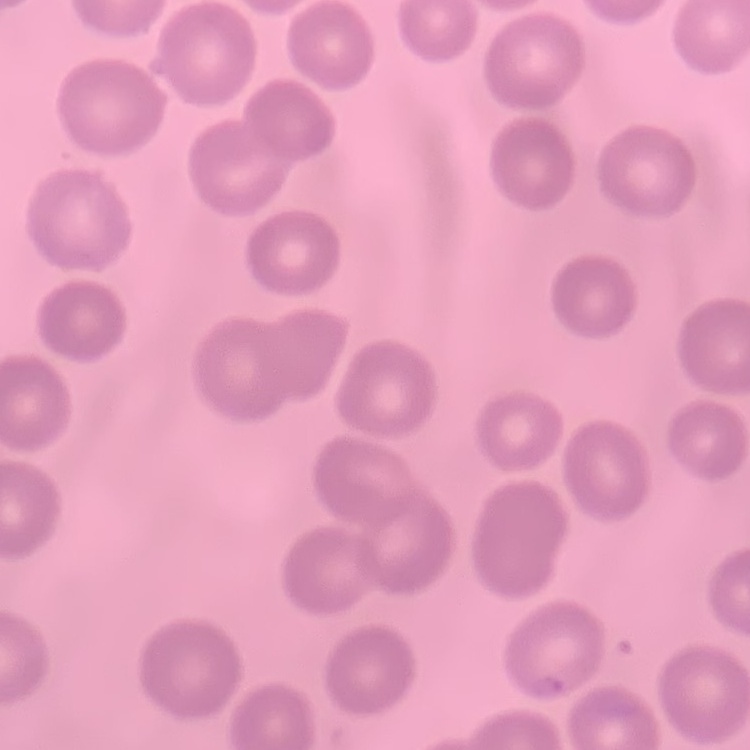
The red blood cells exhibit no rouleaux formation. Square crop of a larger photomicrograph. Thin blood film. Field's or Giemsa stain.